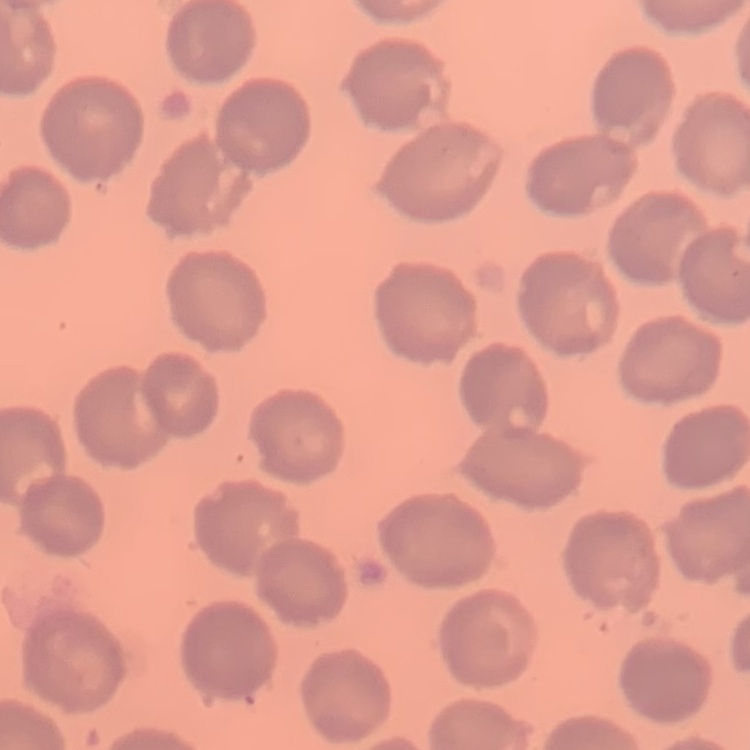

The erythrocytes exhibit no rouleaux formation. Stained with either Field's or Giemsa. Square crop of a larger photomicrograph. Thin blood film.